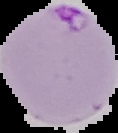
Result: malaria parasites detected. Image is 118×133 pixels. Segmented cell region on a black background. From a thin blood film.